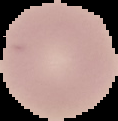
{
  "result": "no Plasmodium parasites seen",
  "image_type": "segmented cell region with the area outside set to black",
  "preparation": "thin blood film",
  "image_size": "118×121 pixels"
}